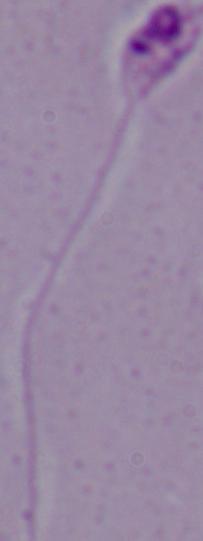

Summary:
  - Identification: Leishmania
  - Modality: micrograph
  - Magnification: 1000x